Name the cell type shown.
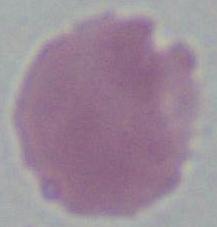

An erythrocyte.

modality: micrograph
magnification: 1000x